Assess the morphology of the red blood cells.
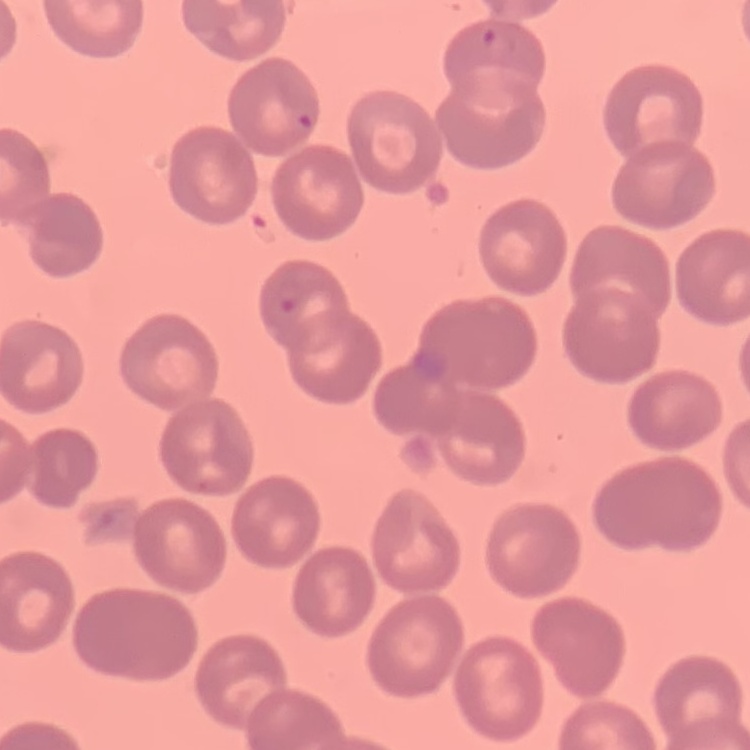
They show no rouleaux formation.

One tile cut from a larger photomicrograph. Stained with either Field's or Giemsa. Thin blood film.